Locate and identify every blood parasite.
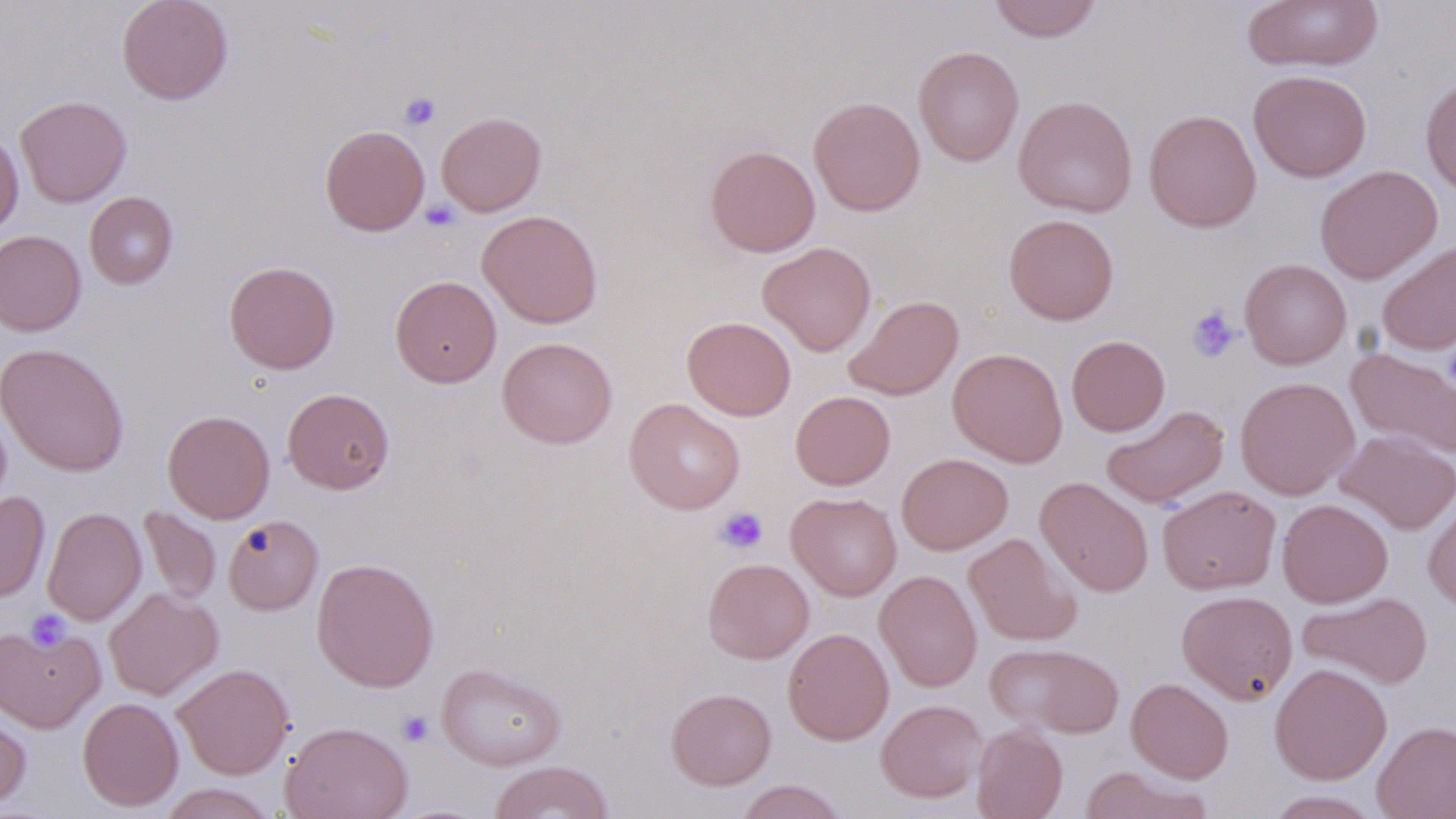

No blood parasites observed.

slide-level diagnosis = negative for blood parasites
field of view = one of a larger specimen
image size = 1456×819 pixels
modality = light microscopy
magnification = 1000x
stain = May-Grünwald-Giemsa
preparation = thin blood film
uninfected red blood cell locations = approximate bounding boxes as named x1/y1/x2/y2 corners in pixels: (x1=116, y1=0, x2=234, y2=105), (x1=988, y1=0, x2=1103, y2=42), (x1=1242, y1=1, x2=1383, y2=72), (x1=913, y1=46, x2=1024, y2=166), (x1=1248, y1=69, x2=1372, y2=182), (x1=1420, y1=75, x2=1456, y2=196), (x1=15, y1=95, x2=132, y2=207), (x1=1014, y1=95, x2=1138, y2=218), (x1=808, y1=96, x2=925, y2=216), (x1=1143, y1=109, x2=1262, y2=233), (x1=435, y1=111, x2=546, y2=217), (x1=319, y1=124, x2=430, y2=236), (x1=0, y1=130, x2=24, y2=235), (x1=704, y1=144, x2=821, y2=258), (x1=1315, y1=165, x2=1442, y2=283), (x1=84, y1=191, x2=178, y2=289), (x1=477, y1=210, x2=603, y2=329), (x1=1003, y1=213, x2=1119, y2=325), (x1=0, y1=230, x2=86, y2=336), (x1=1377, y1=240, x2=1456, y2=355), (x1=757, y1=241, x2=876, y2=356), (x1=1239, y1=259, x2=1352, y2=370), (x1=223, y1=260, x2=340, y2=374), (x1=390, y1=275, x2=501, y2=388), (x1=844, y1=294, x2=963, y2=401), (x1=682, y1=316, x2=796, y2=421), (x1=1066, y1=335, x2=1170, y2=436), (x1=497, y1=337, x2=617, y2=448), (x1=1, y1=343, x2=129, y2=476), (x1=1345, y1=346, x2=1456, y2=461), (x1=948, y1=348, x2=1068, y2=467), (x1=1234, y1=377, x2=1359, y2=499), (x1=282, y1=388, x2=395, y2=494), (x1=790, y1=390, x2=895, y2=490), (x1=624, y1=398, x2=745, y2=515), (x1=1101, y1=404, x2=1229, y2=509), (x1=162, y1=409, x2=275, y2=523), (x1=1336, y1=430, x2=1456, y2=534), (x1=897, y1=453, x2=1013, y2=555), (x1=1035, y1=477, x2=1153, y2=597), (x1=1157, y1=485, x2=1281, y2=595), (x1=0, y1=491, x2=50, y2=603), (x1=787, y1=492, x2=901, y2=600), (x1=1423, y1=495, x2=1456, y2=613), (x1=1277, y1=498, x2=1393, y2=608), (x1=42, y1=506, x2=146, y2=625), (x1=138, y1=506, x2=222, y2=605), (x1=223, y1=515, x2=323, y2=615), (x1=964, y1=533, x2=1081, y2=646), (x1=311, y1=557, x2=439, y2=692), (x1=702, y1=558, x2=814, y2=663), (x1=874, y1=570, x2=982, y2=692), (x1=104, y1=587, x2=223, y2=700), (x1=1176, y1=590, x2=1298, y2=704), (x1=1297, y1=591, x2=1433, y2=688), (x1=0, y1=622, x2=105, y2=732), (x1=782, y1=627, x2=894, y2=745), (x1=985, y1=643, x2=1124, y2=738), (x1=436, y1=662, x2=567, y2=770), (x1=172, y1=663, x2=294, y2=780), (x1=1269, y1=663, x2=1392, y2=784), (x1=1126, y1=677, x2=1234, y2=783), (x1=666, y1=687, x2=776, y2=790), (x1=77, y1=697, x2=183, y2=812), (x1=876, y1=699, x2=987, y2=803), (x1=0, y1=701, x2=32, y2=811), (x1=280, y1=721, x2=413, y2=819), (x1=1372, y1=721, x2=1456, y2=819), (x1=971, y1=724, x2=1067, y2=819), (x1=488, y1=761, x2=615, y2=819), (x1=1080, y1=766, x2=1211, y2=819), (x1=733, y1=780, x2=850, y2=819), (x1=156, y1=783, x2=280, y2=818), (x1=1265, y1=790, x2=1383, y2=818)
platelet locations = approximate bounding boxes as named x1/y1/x2/y2 corners in pixels: (x1=399, y1=92, x2=441, y2=130), (x1=420, y1=198, x2=461, y2=232), (x1=1186, y1=306, x2=1240, y2=363), (x1=1443, y1=342, x2=1456, y2=394), (x1=714, y1=506, x2=769, y2=554), (x1=26, y1=610, x2=71, y2=652), (x1=397, y1=711, x2=433, y2=746)